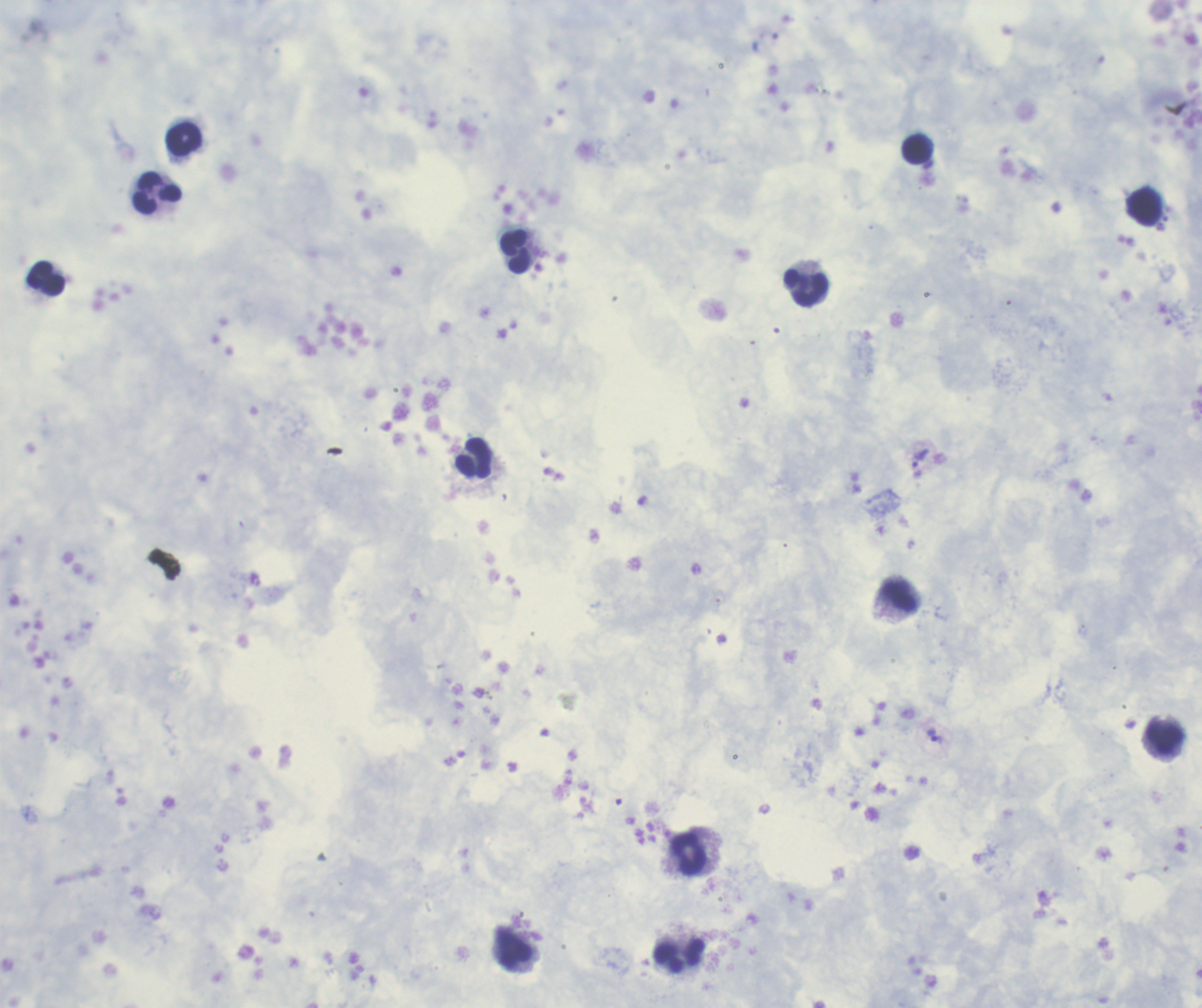
Approximate centers as {x, y} in pixels.
Summary:
  - Trophozoite locations: {921, 458}, {934, 736}
  - Leukocyte locations: {183, 140}, {916, 150}, {157, 194}, {1144, 206}, {516, 251}, {45, 278}, {807, 287}, {473, 457}, {899, 597}, {1165, 739}, {691, 854}, {515, 948}, {679, 955}
  - Field of view: one from this slide
  - Magnification: 100x
  - Preparation: thick blood smear
  - Image size: 1202×1008 pixels
  - Stain: Romanowsky
  - Result: Plasmodium parasites identified
  - Coloration quality: good
  - Context: previously used in an actual diagnosis
  - Background quality: unsatisfactory